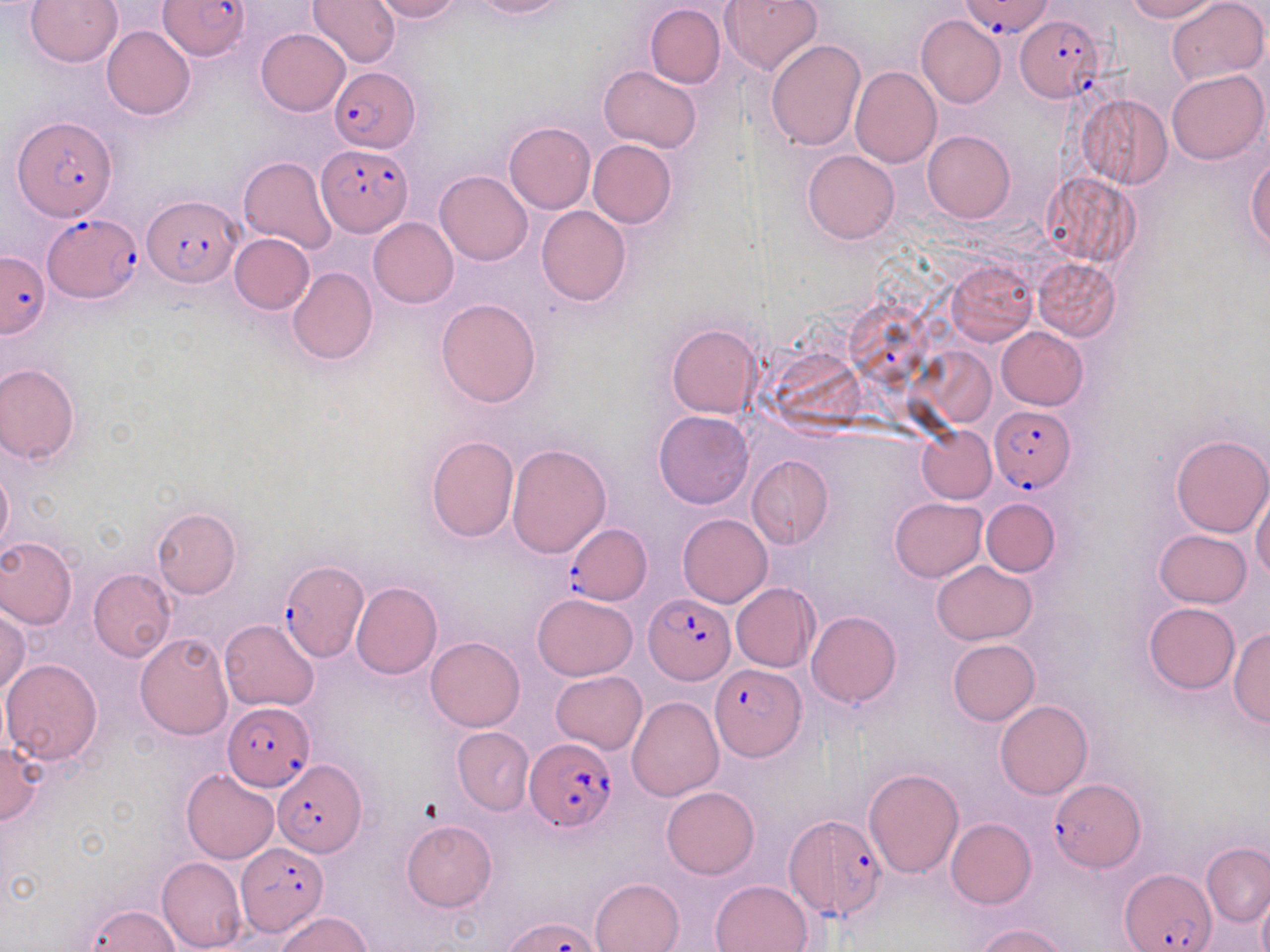
slide-level diagnosis = Plasmodium falciparum
uninfected red blood cell locations = approximate bounding boxes as (x1,y1)-(x2,y2) corner pairs in pixels: (26,0)-(122,68), (306,0)-(400,69), (372,0)-(461,22), (470,0)-(568,19), (726,0)-(821,76), (1122,0)-(1220,22), (1166,0)-(1266,86), (645,3)-(727,88), (916,14)-(1005,108), (101,26)-(195,120), (256,28)-(350,116), (766,39)-(867,151), (599,65)-(702,153), (850,66)-(941,167), (1167,68)-(1268,165), (1077,94)-(1172,188), (504,121)-(595,213), (923,130)-(1015,223), (587,140)-(677,228), (803,150)-(900,244), (239,156)-(336,253), (1246,156)-(1270,250), (435,171)-(533,266), (1041,173)-(1140,266), (535,205)-(632,308), (369,217)-(459,308), (230,234)-(315,314), (947,258)-(1037,346), (1033,258)-(1120,341), (287,268)-(378,365), (435,297)-(542,408), (666,323)-(763,419), (997,327)-(1088,409), (921,347)-(998,428), (0,363)-(79,465), (654,410)-(753,509), (917,425)-(996,503), (1169,434)-(1270,539), (426,435)-(518,540), (507,442)-(612,558), (747,455)-(833,549), (0,463)-(12,556), (1251,487)-(1270,582), (889,497)-(987,581), (980,498)-(1060,576), (150,506)-(240,598), (679,514)-(773,607), (1154,529)-(1252,607), (0,536)-(77,630), (932,561)-(1037,644), (88,568)-(175,661), (351,582)-(442,679), (731,583)-(820,672), (533,593)-(637,680), (1144,602)-(1240,694), (0,608)-(30,696), (807,611)-(901,708), (219,619)-(319,711), (1230,626)-(1270,728), (135,633)-(234,740), (425,637)-(524,732), (948,639)-(1040,726), (1,657)-(104,764), (551,671)-(647,753), (627,697)-(723,801), (995,701)-(1092,799), (452,726)-(535,815), (0,741)-(43,825), (863,768)-(964,878), (181,769)-(279,863), (661,785)-(759,879), (946,817)-(1036,908), (401,820)-(495,912), (1201,843)-(1269,925), (157,855)-(245,952), (591,878)-(684,952), (710,879)-(814,952), (1257,888)-(1270,952), (86,904)-(182,951), (275,912)-(374,952), (974,923)-(1070,952)
field of view = one of a larger specimen
Plasmodium falciparum-infected red blood cell locations = approximate bounding boxes as (x1,y1)-(x2,y2) corner pairs in pixels: (159,0)-(250,61), (961,0)-(1054,38), (1016,14)-(1102,101), (331,69)-(417,153), (13,115)-(116,220), (316,143)-(413,236), (142,194)-(243,289), (42,215)-(144,302), (0,252)-(50,338), (989,406)-(1076,491), (568,524)-(651,603), (278,557)-(369,661), (644,596)-(733,685), (710,664)-(805,760), (223,702)-(315,791), (524,737)-(619,833), (272,758)-(366,855), (1049,777)-(1143,872), (785,817)-(887,926), (237,841)-(328,938), (1122,869)-(1215,952), (507,916)-(603,952)
preparation = thin blood smear
magnification = 1000x
modality = optical microscopy
stain = May-Grünwald-Giemsa
image size = 1270×952 pixels